Comment on the morphology of the erythrocytes.
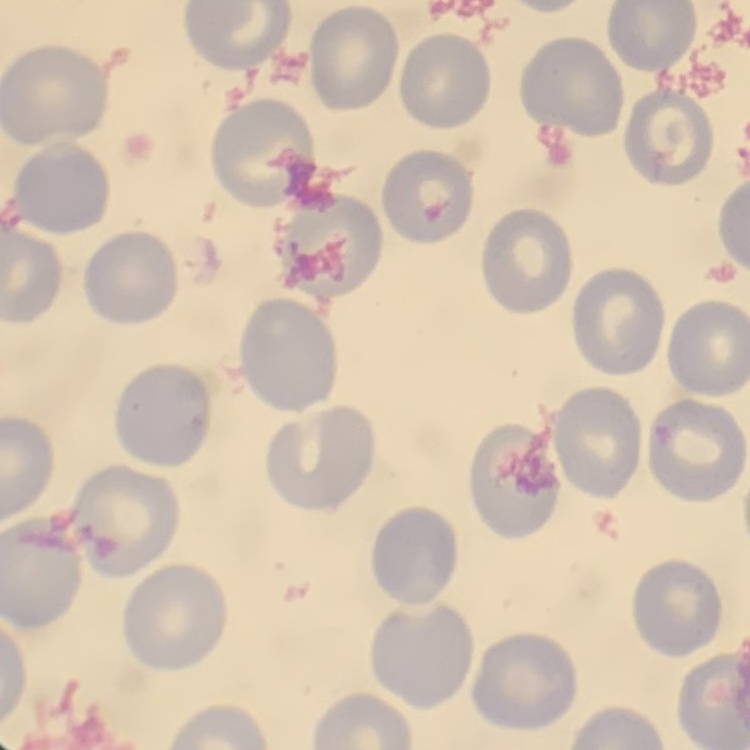
They show no rouleaux formation.

stain = Field's or Giemsa
preparation = thin peripheral smear
image type = one tile cut from a larger photomicrograph